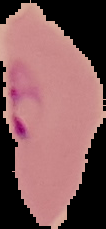 From a thin blood film. Image is 106×229 pixels. Result: Plasmodium parasites identified. Cell region segmented out of the field of view; the surrounding area is masked to black.